Assess this cell for malaria.
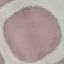

It is uninfected.

Summary:
  - Stain: Giemsa
  - Capture: smartphone through the microscope eyepiece
  - Preparation: thin blood smear
  - Image type: automatically extracted cell patch, resized to 64 × 64 pixels